Locate every Plasmodium malariae-infected red blood cell.
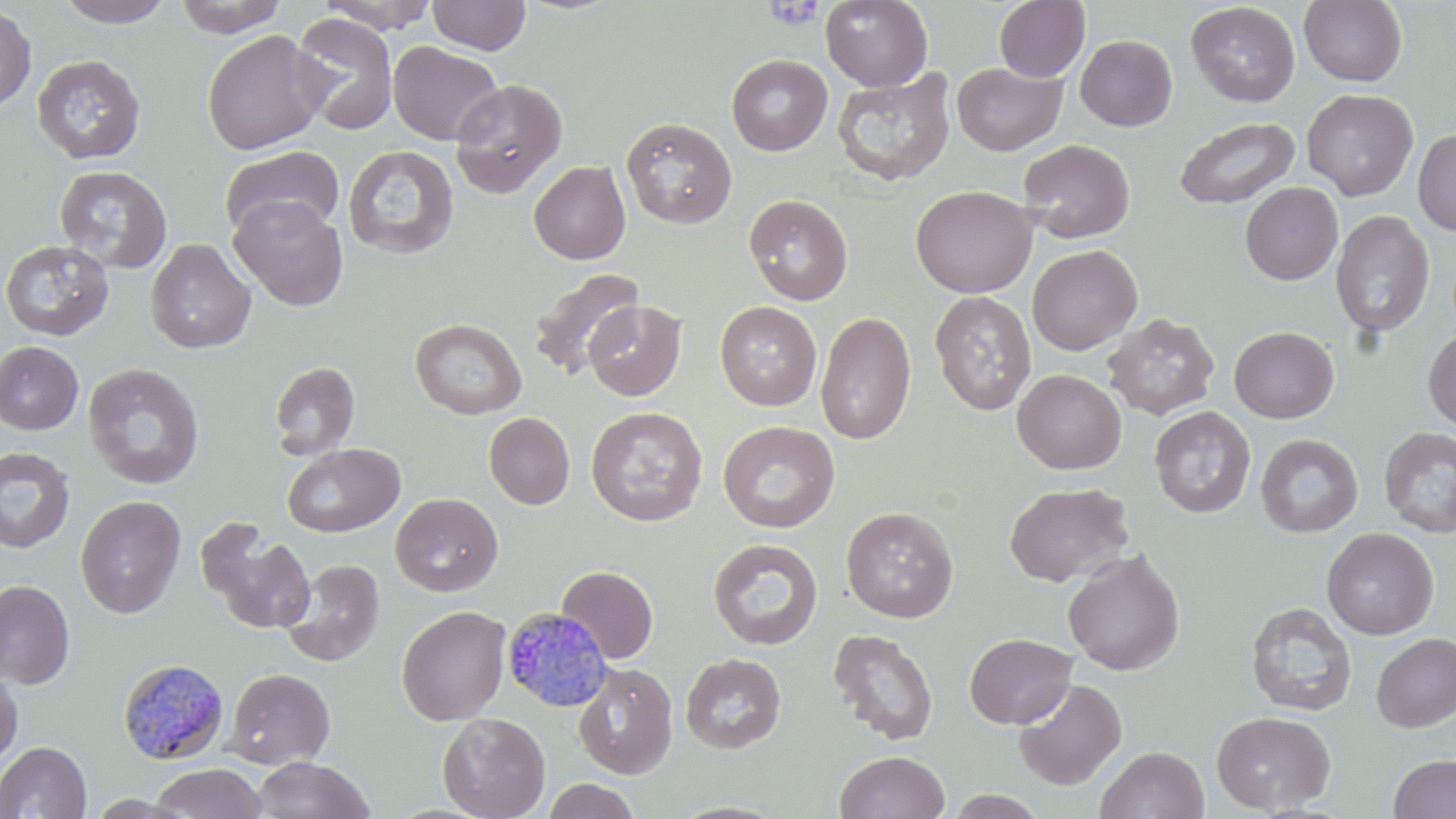
Approximate bounding boxes as (x1, y1, x2, y2) in pixels.
Plasmodium malariae-infected red blood cells: (502, 607, 614, 712), (118, 658, 230, 767).

slide_level_diagnosis: Plasmodium malariae
uninfected_red_blood_cell_locations: 'approximate bounding boxes as (x1, y1, x2, y2) in pixels: (53, 0, 177, 27), (174, 0, 290, 38), (427, 0, 531, 56), (820, 0, 933, 91), (1299, 0, 1407, 87), (318, 1, 440, 34), (994, 1, 1090, 82), (1185, 2, 1300, 107), (0, 5, 37, 113), (289, 12, 399, 136), (202, 30, 330, 155), (1075, 35, 1178, 131), (388, 41, 504, 146), (31, 54, 146, 165), (726, 54, 833, 156), (952, 62, 1067, 156), (831, 69, 957, 187), (449, 78, 568, 198), (1301, 88, 1418, 201), (621, 116, 737, 229), (1174, 117, 1300, 210), (1413, 127, 1456, 236), (1018, 139, 1136, 243), (343, 144, 460, 261), (218, 145, 345, 240), (528, 161, 631, 265), (54, 164, 172, 274), (1240, 182, 1342, 285), (911, 185, 1036, 298), (743, 193, 854, 305), (228, 195, 349, 311), (1330, 210, 1435, 339), (145, 238, 256, 354), (0, 239, 114, 340), (1027, 244, 1143, 355), (527, 267, 645, 381), (929, 290, 1036, 416), (584, 300, 686, 401), (715, 301, 822, 411), (815, 311, 915, 445), (1103, 312, 1219, 420), (410, 318, 527, 419), (1229, 326, 1339, 423), (1422, 328, 1456, 431), (0, 341, 83, 435), (268, 360, 360, 463), (82, 363, 205, 489), (1013, 369, 1127, 474), (1149, 405, 1255, 518), (586, 406, 708, 526), (483, 412, 575, 510), (717, 420, 840, 533), (1379, 426, 1456, 537), (1255, 433, 1363, 538), (282, 443, 405, 537), (0, 445, 75, 554), (1004, 482, 1134, 587), (390, 492, 504, 596), (75, 495, 186, 619), (840, 505, 959, 623), (197, 518, 316, 635), (1321, 527, 1439, 639), (708, 538, 823, 651), (1062, 549, 1185, 676), (281, 559, 384, 667), (556, 565, 658, 663), (0, 580, 75, 689), (1245, 602, 1357, 717), (396, 605, 511, 726), (827, 628, 940, 746), (964, 632, 1077, 729), (1371, 633, 1456, 732), (680, 653, 786, 754), (573, 662, 678, 779), (223, 668, 335, 769), (0, 669, 23, 771), (1012, 678, 1127, 790), (1211, 710, 1336, 814), (437, 712, 550, 819), (0, 741, 92, 818), (1095, 746, 1209, 819), (834, 750, 950, 819), (1388, 753, 1456, 818), (250, 756, 376, 818), (149, 763, 268, 819), (542, 778, 640, 819), (945, 790, 1049, 818)'
preparation: thin blood film
stain: May-Grünwald-Giemsa
field_of_view: one of a larger specimen
magnification: 1000x
modality: light microscopy
platelet_locations: 'approximate bounding boxes as (x1, y1, x2, y2) in pixels: (764, 1, 825, 30)'
image_size: 1456×819 pixels